Give the extent of all uninfected red blood cells.
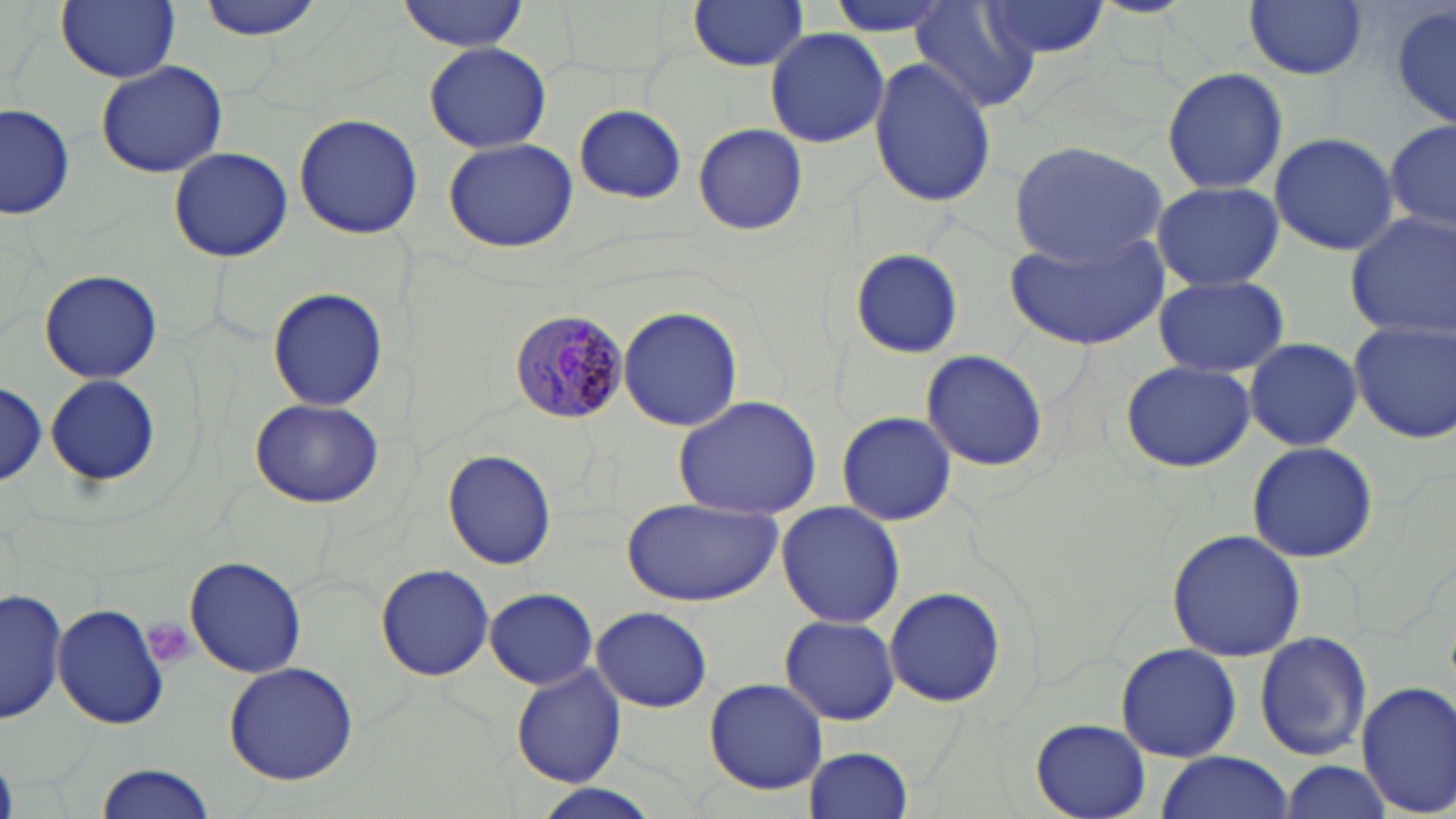
Approximate bounding boxes as (x1, y1, x2, y2) in pixels.
Uninfected red blood cells: (57, 0, 179, 83), (195, 0, 329, 40), (398, 0, 527, 52), (687, 0, 810, 71), (821, 0, 960, 39), (982, 0, 1109, 61), (1245, 0, 1369, 80), (913, 2, 1039, 114), (1389, 4, 1455, 133), (765, 27, 889, 150), (423, 42, 552, 154), (869, 58, 996, 208), (97, 61, 227, 176), (1162, 65, 1288, 195), (1, 103, 75, 220), (572, 105, 688, 203), (293, 113, 423, 239), (1386, 118, 1456, 236), (693, 123, 807, 236), (1269, 131, 1398, 256), (442, 138, 579, 254), (1008, 140, 1169, 265), (168, 145, 291, 260), (1151, 179, 1284, 292), (1343, 210, 1456, 343), (1004, 228, 1169, 351), (847, 248, 965, 358), (39, 269, 163, 384), (1154, 274, 1288, 378), (1140, 279, 1276, 469), (266, 285, 391, 409), (617, 305, 744, 431), (1350, 319, 1455, 445), (1243, 337, 1362, 451), (919, 348, 1050, 470), (1120, 360, 1255, 473), (45, 373, 158, 488), (0, 380, 47, 488), (672, 395, 822, 519), (249, 397, 384, 509), (836, 411, 957, 527), (1246, 441, 1379, 564), (442, 447, 557, 571), (620, 496, 781, 606), (776, 503, 906, 628), (1166, 529, 1308, 663), (184, 556, 307, 679), (374, 563, 495, 681), (885, 586, 1004, 709), (2, 588, 68, 723), (485, 588, 600, 690), (51, 603, 171, 730), (590, 606, 712, 712), (778, 615, 902, 727), (1253, 632, 1373, 762), (1115, 644, 1243, 761), (223, 662, 359, 786), (510, 666, 628, 787), (702, 677, 828, 795), (1355, 678, 1456, 818), (1032, 718, 1151, 818), (806, 746, 913, 817), (1153, 752, 1296, 819), (1279, 760, 1392, 816), (93, 761, 219, 819), (531, 786, 661, 818).

Platelet locations: (139, 618, 199, 670). Plasmodium malariae-infected red blood cell locations: (508, 311, 629, 422). Slide-level diagnosis: Plasmodium malariae. Image is 1456×819 pixels. Light microscopy. Thin blood film. Single field of view. 1000x magnification. May-Grünwald-Giemsa stain.